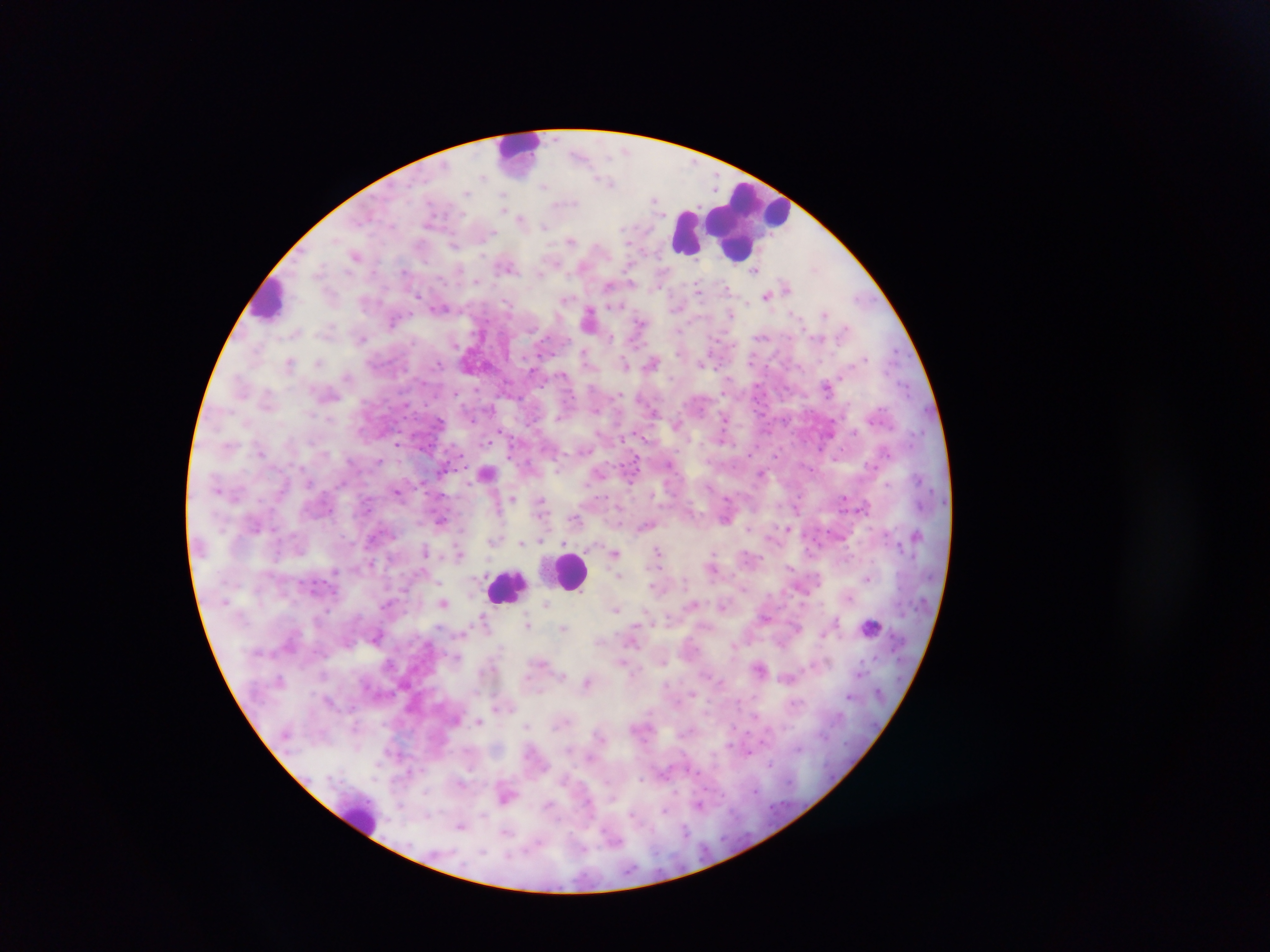
{
  "capture": "mobile-phone photograph through a microscope",
  "image_size": "1270×952 pixels",
  "preparation": "thick blood film",
  "country": "Ghana",
  "leukocyte_locations": "approximate centers as {x, y} in pixels: {522, 145}, {750, 222}, {684, 234}, {271, 299}, {570, 570}, {501, 587}, {359, 815}",
  "malaria_parasite_locations": "approximate centers as {x, y} in pixels: {580, 156}, {483, 177}, {610, 185}, {542, 187}, {466, 193}, {504, 196}, {656, 202}, {565, 203}, {522, 219}, {542, 225}, {490, 234}, {570, 240}, {630, 243}, {454, 244}, {355, 254}, {505, 267}, {544, 270}, {406, 272}, {478, 283}, {697, 287}, {609, 288}, {725, 288}, {415, 295}, {766, 295}, {858, 299}, {566, 300}, {508, 301}, {676, 306}, {440, 307}, {588, 314}, {824, 315}, {393, 322}, {638, 323}, {362, 338}, {457, 342}, {584, 354}, {653, 361}, {288, 362}, {320, 363}, {625, 363}, {703, 363}, {438, 365}, {532, 366}, {347, 376}, {827, 385}, {905, 385}, {476, 389}, {616, 396}, {470, 413}, {560, 414}, {331, 420}, {724, 431}, {830, 432}, {487, 439}, {398, 444}, {885, 449}, {587, 450}, {670, 462}, {378, 463}, {560, 463}, {634, 464}, {872, 464}, {808, 467}, {486, 472}, {765, 473}, {306, 482}, {886, 483}, {341, 484}, {398, 492}, {657, 493}, {512, 496}, {846, 497}, {729, 500}, {542, 502}, {867, 507}, {574, 518}, {440, 520}, {726, 520}, {254, 526}, {646, 526}, {788, 527}, {750, 529}, {496, 540}, {523, 543}, {299, 548}, {425, 548}, {459, 549}, {658, 550}, {615, 551}, {712, 554}, {790, 566}, {334, 570}, {622, 575}, {867, 578}, {437, 581}, {850, 598}, {444, 602}, {723, 604}, {546, 605}, {692, 605}, {616, 609}, {767, 618}, {484, 619}, {838, 624}, {872, 624}, {528, 625}, {795, 627}, {564, 629}, {377, 636}, {633, 642}, {457, 657}, {664, 660}, {621, 661}, {827, 662}, {544, 663}, {861, 666}, {860, 673}, {562, 677}, {787, 679}, {588, 681}, {692, 692}, {851, 695}, {331, 703}, {479, 720}, {527, 726}, {748, 750}, {590, 758}, {770, 764}, {639, 778}, {758, 790}, {725, 798}, {703, 805}, {666, 813}, {429, 815}, {631, 815}, {460, 828}, {686, 830}",
  "field_of_view": "single"
}